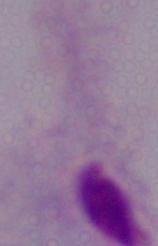

identification: trichomonad
magnification: 1000x
modality: photomicrograph